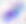

Toxoplasma gondii is seen. Captured at 400x magnification. Micrograph.